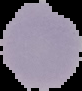
image size = 82×91 pixels
malaria status = uninfected
image type = cell region segmented out of the field of view; surrounding area masked to black
preparation = thin blood smear